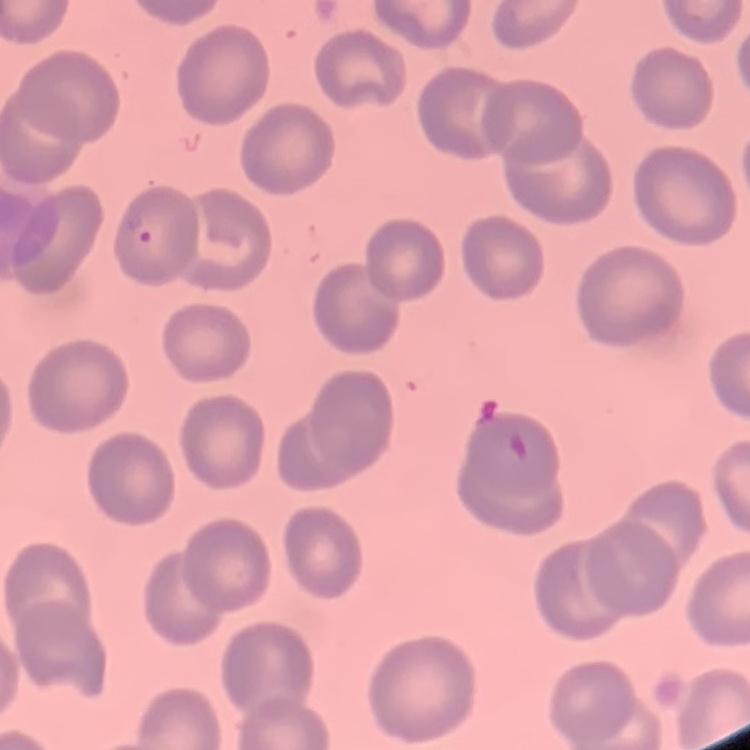 The red blood cells exhibit no rouleaux formation. Thin blood film. Field's or Giemsa stain. One tile cut from a larger photomicrograph.